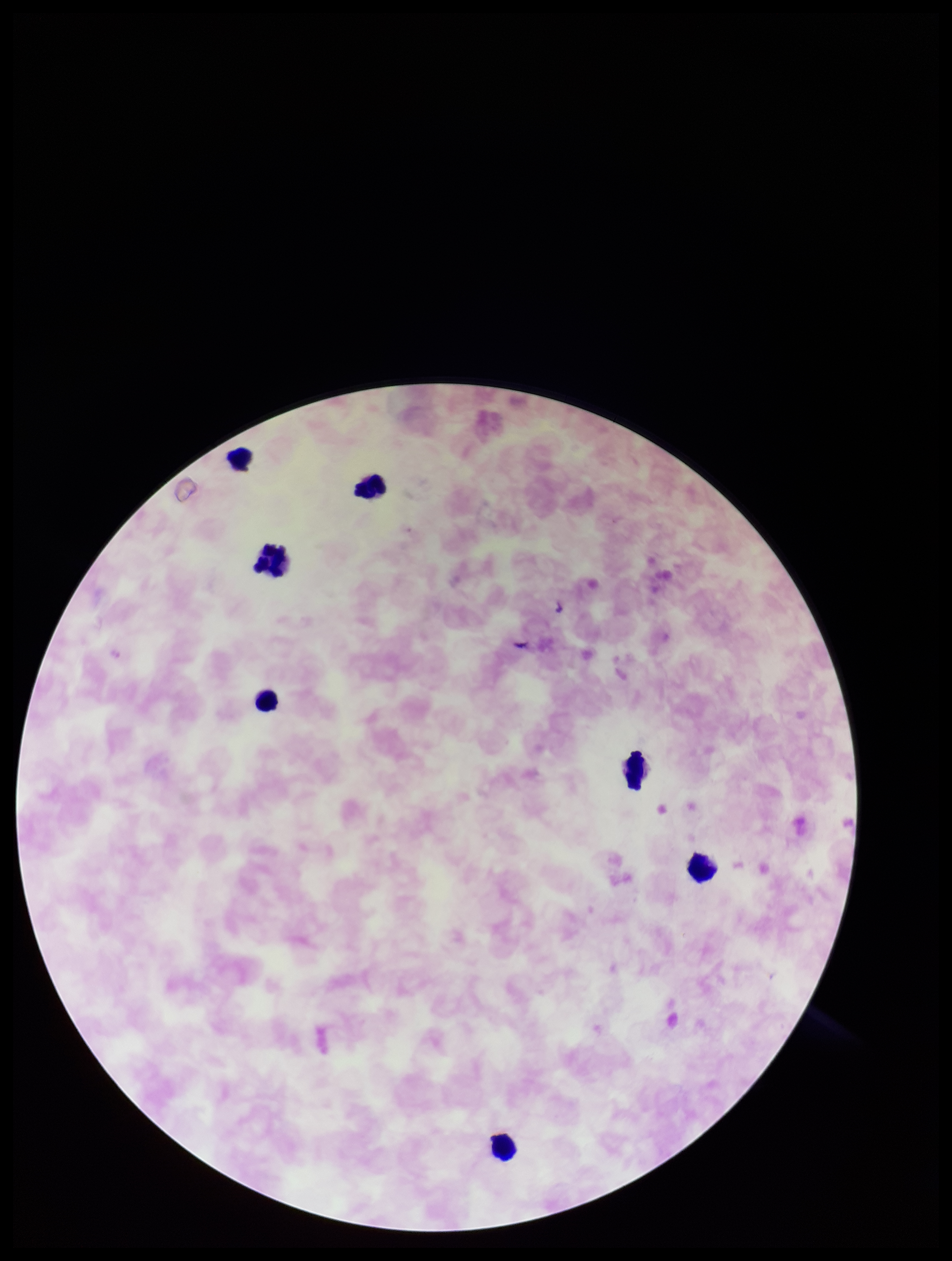 Leukocyte count: 7. Patient malaria status: positive. Image is 952×1261 pixels. Species reported for this patient: Plasmodium falciparum. Plasmodium parasites: none detected. Photographed through the microscope eyepiece with a smartphone camera. Preparation: thick smear. Stained with Giemsa. Parasite count: 0. One field from this slide.